Classify this cell by malaria status.
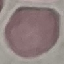
It is uninfected.

Summary:
  - Preparation: thin smear
  - Stain: Giemsa
  - Image type: cell patch, automatically extracted from a larger field of view and resized to 64 × 64 pixels
  - Capture: smartphone camera at the microscope eyepiece